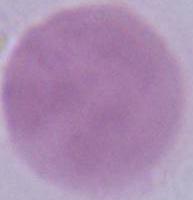

An erythrocyte is shown. Photomicrograph. 1000x magnification.